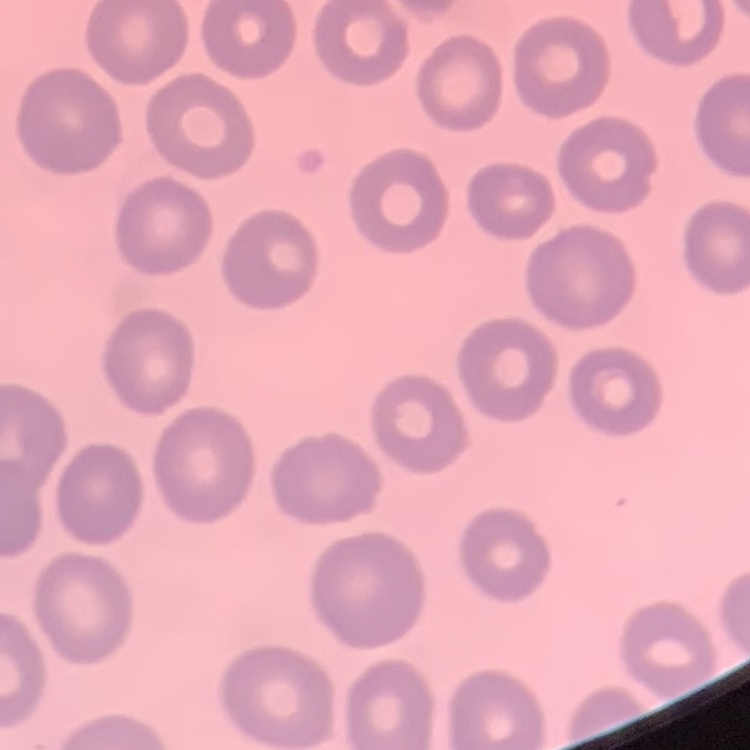

Summary:
  - Red blood cell morphology: no rouleaux formation
  - Stain: Field's or Giemsa
  - Preparation: thin peripheral smear
  - Image type: square crop of a larger photomicrograph